Assess the morphology of the red blood cells.
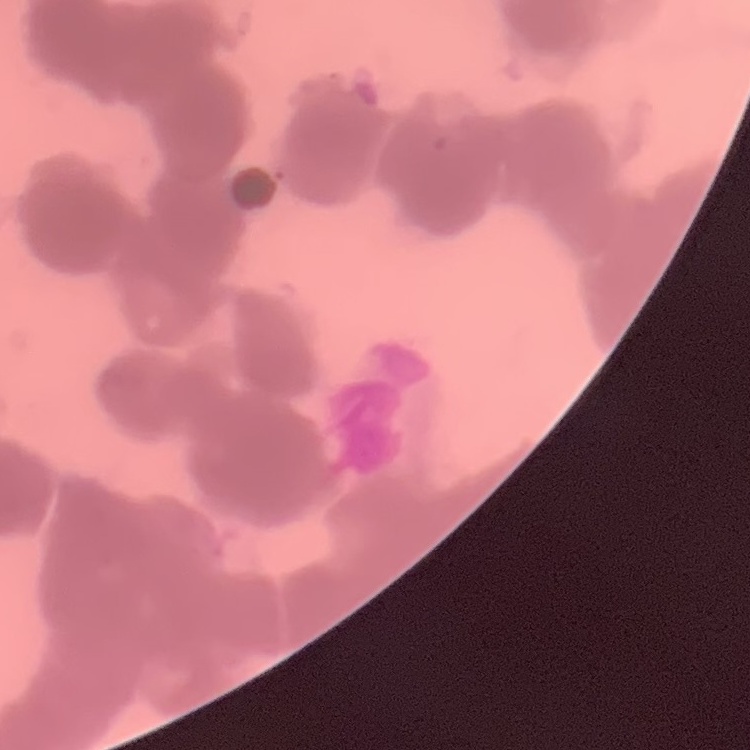
Rouleaux formation.

image type = square crop of a larger photomicrograph
preparation = thin blood smear
stain = Field's or Giemsa